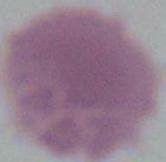

modality: photomicrograph
identification: red blood cell
magnification: 1000x